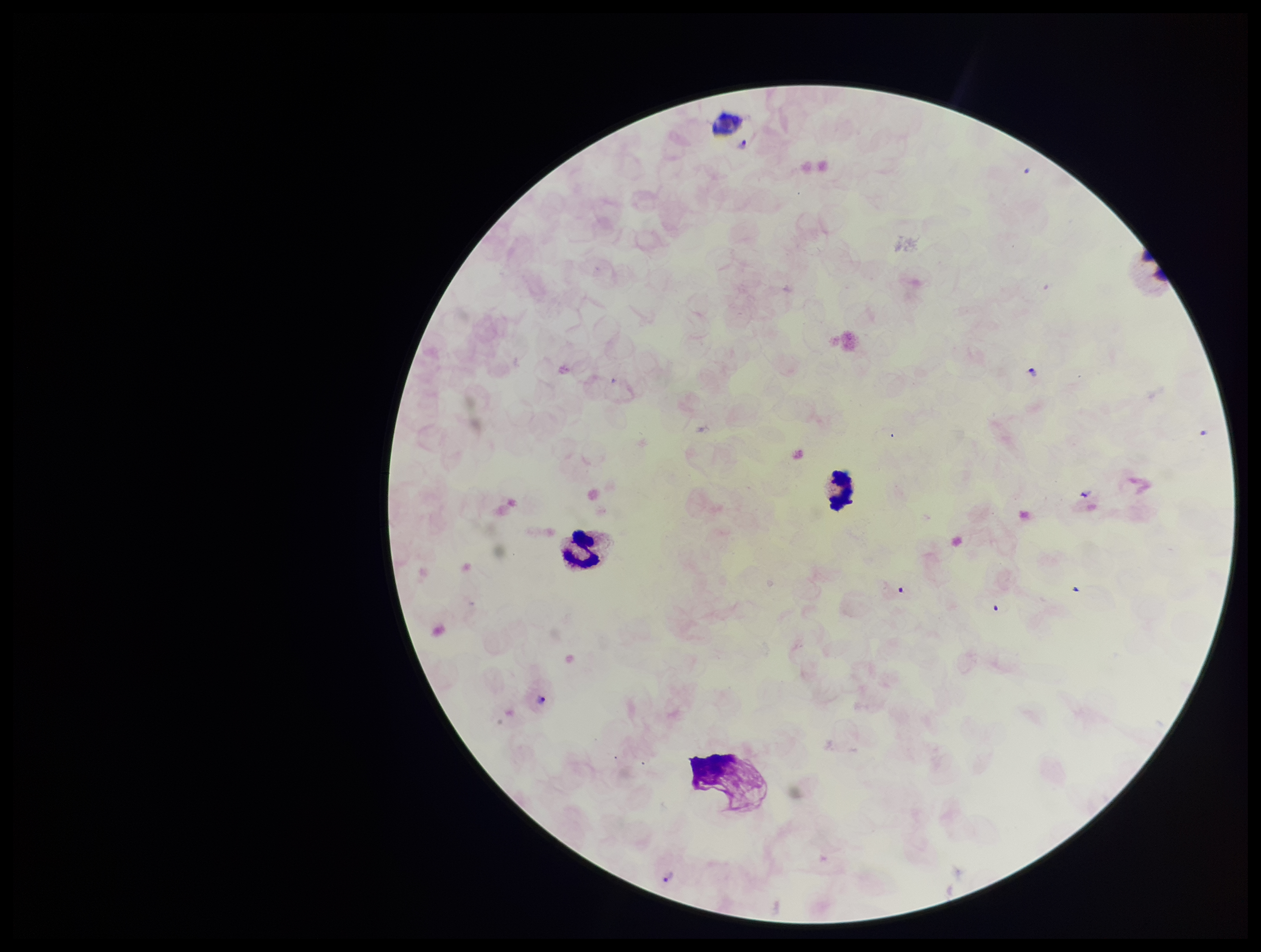

image_size: 1261×952 pixels
preparation: thick blood smear
stain: Giemsa
parasite_count: 4
leukocyte_count: 3
field_of_view: single
plasmodium_parasites: seen
capture: smartphone photograph through the microscope eyepiece
species_reported_for_this_patient: Plasmodium vivax
patient_malaria_status: infected